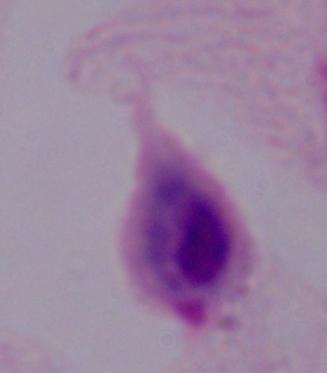

Summary:
  - Modality: photomicrograph
  - Identification: trichomonad
  - Magnification: 1000x